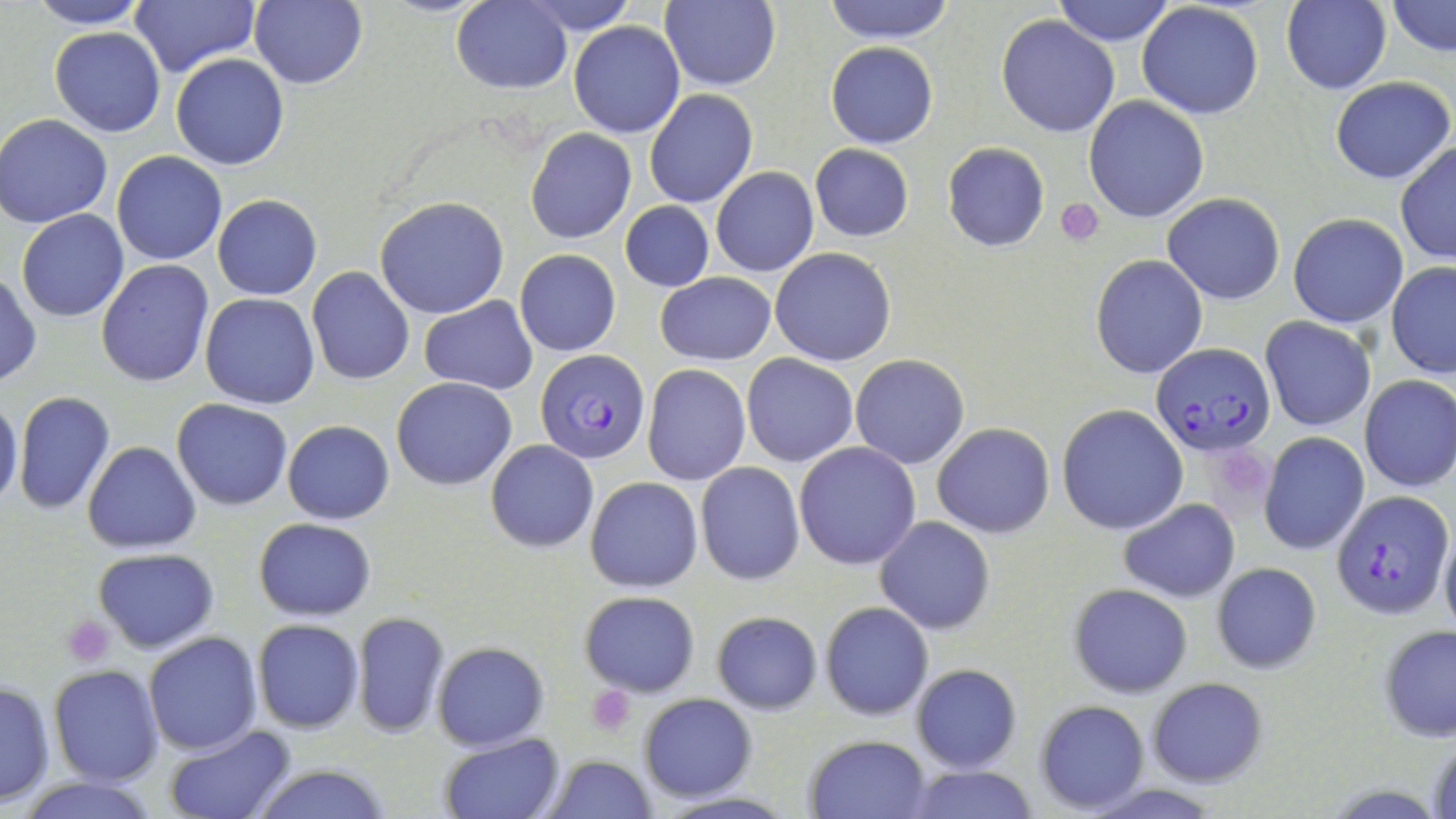
slide-level diagnosis = Plasmodium falciparum
magnification = 1000x
Plasmodium falciparum-infected red blood cell locations = approximate bounding boxes as (x1,y1)-(x2,y2) corner pairs in pixels: (1152,345)-(1275,457), (537,347)-(649,462), (1332,489)-(1453,619)
uninfected red blood cell locations = approximate bounding boxes as (x1,y1)-(x2,y2) corner pairs in pixels: (26,0)-(152,29), (129,0)-(257,78), (450,0)-(573,95), (661,0)-(781,92), (825,0)-(955,44), (1052,0)-(1175,46), (1282,0)-(1392,95), (248,1)-(368,89), (525,1)-(636,35), (1135,1)-(1264,120), (1388,1)-(1454,55), (996,15)-(1122,138), (569,20)-(685,138), (50,25)-(165,137), (825,43)-(938,148), (170,53)-(289,171), (1330,75)-(1454,184), (643,90)-(756,209), (1083,95)-(1211,223), (0,113)-(113,229), (524,128)-(636,245), (1395,140)-(1456,265), (942,142)-(1049,252), (809,143)-(913,241), (112,151)-(226,266), (711,168)-(819,278), (1161,192)-(1285,305), (213,194)-(322,300), (374,197)-(509,319), (620,200)-(715,292), (17,210)-(128,322), (1289,213)-(1409,327), (770,246)-(897,366), (515,249)-(620,356), (1090,255)-(1208,379), (96,260)-(214,387), (1386,263)-(1456,379), (306,266)-(414,385), (655,271)-(776,366), (0,272)-(41,388), (202,293)-(319,408), (419,295)-(537,395), (1261,317)-(1376,431), (742,353)-(858,467), (850,354)-(970,469), (642,364)-(751,486), (1358,373)-(1456,492), (391,377)-(517,490), (13,391)-(115,516), (0,396)-(24,512), (173,399)-(291,510), (1057,404)-(1188,535), (282,419)-(395,524), (931,423)-(1056,537), (1259,431)-(1368,555), (485,440)-(598,552), (82,441)-(201,553), (794,442)-(922,569), (695,461)-(804,584), (586,477)-(704,591), (1118,498)-(1240,603), (876,516)-(996,636), (253,518)-(376,619), (1439,523)-(1456,641), (92,547)-(219,653), (1210,563)-(1322,674), (1069,584)-(1193,698), (579,589)-(701,696), (821,601)-(933,721), (710,610)-(822,714), (351,611)-(449,739), (252,619)-(364,734), (1378,623)-(1456,743), (143,631)-(264,755), (432,642)-(549,750), (48,663)-(163,787), (910,664)-(1022,774), (1147,676)-(1269,787), (0,678)-(55,806), (638,693)-(758,803), (1034,700)-(1149,814), (161,724)-(297,819), (438,733)-(565,819), (806,734)-(931,818), (540,753)-(657,819), (245,764)-(395,819), (900,765)-(1040,819), (11,773)-(165,819)
stain = May-Grünwald-Giemsa
preparation = thin blood film
modality = light microscopy
image size = 1456×819 pixels
platelet locations = approximate bounding boxes as (x1,y1)-(x2,y2) corner pairs in pixels: (1057,198)-(1104,247), (1208,447)-(1272,511), (61,616)-(113,668), (586,685)-(636,734)
field of view = one of a larger specimen